Give the position of every Plasmodium parasite.
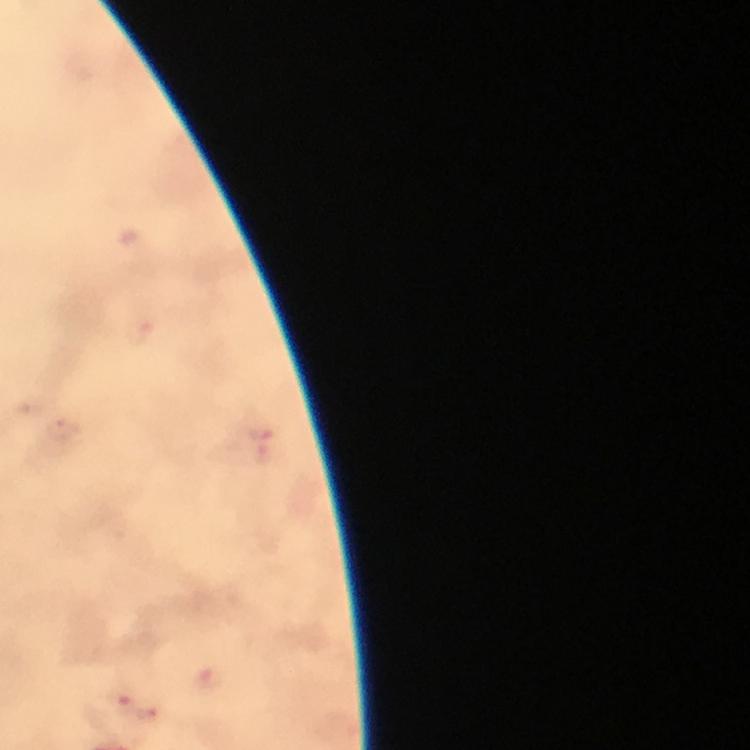

Approximate object centers, in pixels from the top-left corner.
Plasmodium parasites: (x=118, y=698), (x=147, y=716).

Photographed through the microscope with a smartphone camera. A crop from one field of view. From a malaria diagnostic workup. Image is 750×750 pixels. Immersion oil was used. Giemsa stain. Thick blood film. 100x magnification.